Locate every leukocyte (white blood cell).
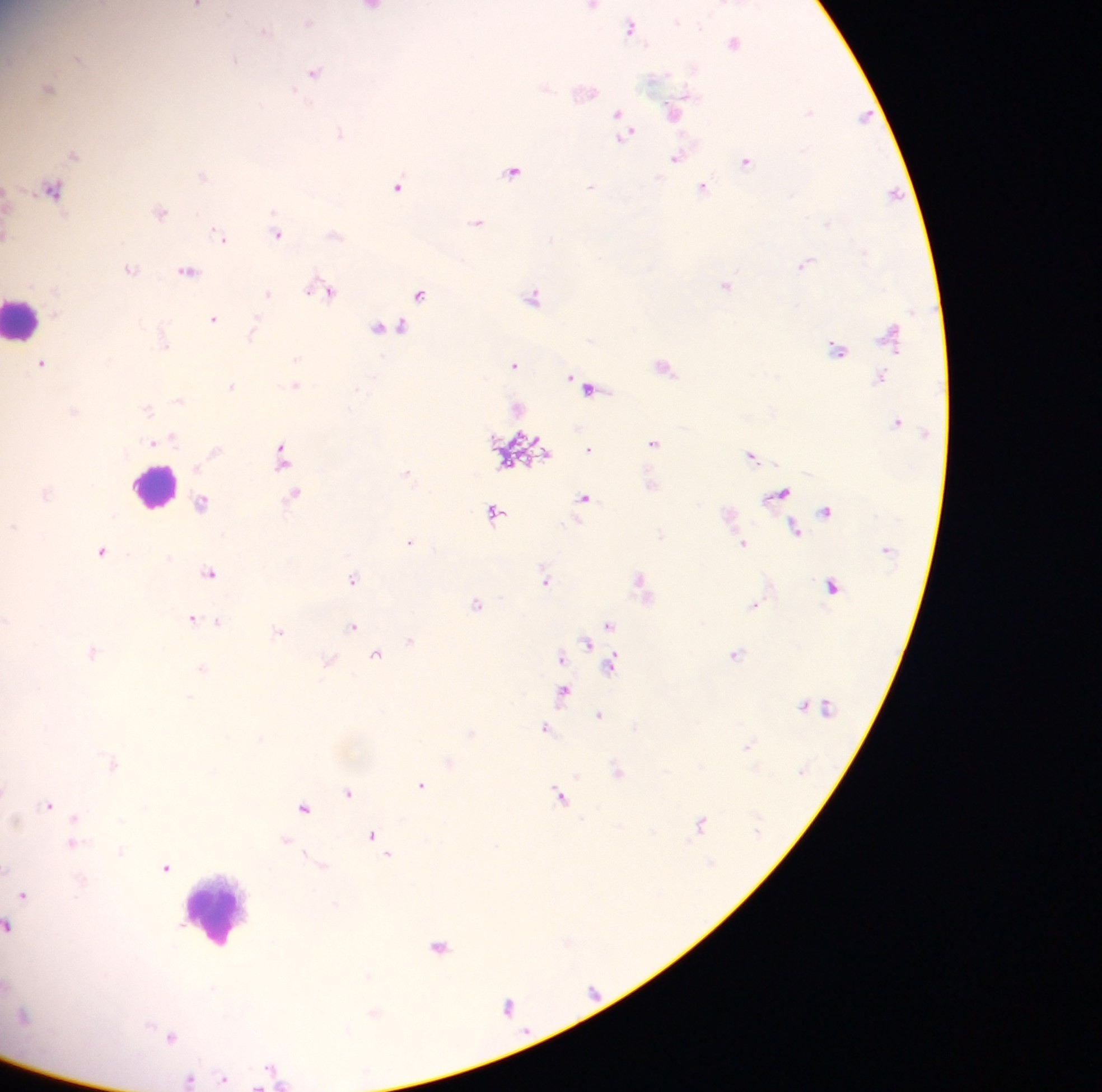
Approximate centers as (x, y) in pixels.
Leukocytes: (25, 322), (150, 488), (218, 916).

capture = mobile-phone photograph through a microscope
preparation = thick blood smear
country = Ghana
malaria parasite locations = approximate centers as (x, y) in pixels: (677, 22), (310, 23), (701, 25), (630, 27), (264, 29), (734, 42), (235, 59), (314, 72), (809, 111), (617, 117), (676, 159), (747, 162), (514, 171), (202, 175), (397, 186), (590, 186), (704, 188), (272, 211), (478, 222), (829, 225), (215, 230), (280, 234), (864, 252), (806, 264), (131, 267), (187, 270), (727, 286), (329, 289), (268, 293), (420, 295), (533, 296), (214, 319), (389, 327), (255, 330), (297, 358), (382, 358), (43, 362), (515, 364), (666, 368), (297, 385), (231, 386), (357, 389), (583, 389), (180, 400), (148, 409), (74, 410), (173, 437), (154, 442), (654, 444), (281, 447), (589, 449), (754, 459), (283, 465), (408, 474), (48, 492), (296, 493), (781, 494), (584, 499), (201, 502), (700, 502), (495, 512), (13, 526), (795, 530), (409, 543), (745, 543), (102, 551), (211, 574), (353, 578), (638, 579), (547, 582), (832, 587), (756, 603), (478, 604), (192, 619), (8, 620), (218, 621), (609, 625), (353, 628), (279, 632), (411, 641), (587, 645), (92, 652), (376, 656), (562, 657), (329, 660), (611, 666), (202, 668), (564, 694), (802, 705), (599, 715), (46, 726), (545, 727), (472, 734), (748, 746), (618, 770), (576, 775), (421, 785), (5, 789), (349, 793), (560, 796), (48, 805), (305, 810), (581, 818), (75, 820), (122, 821), (702, 823), (372, 835), (285, 840), (75, 844), (121, 851), (307, 852), (388, 854), (6, 868), (167, 868), (24, 895), (8, 926), (440, 947), (173, 1035), (270, 1066), (224, 1075), (190, 1078)
image size = 1102×1092 pixels
field of view = single